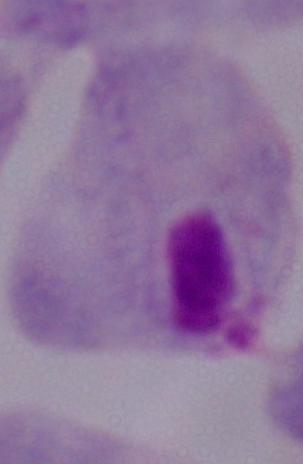
modality = micrograph
identification = trichomonad
magnification = 1000x